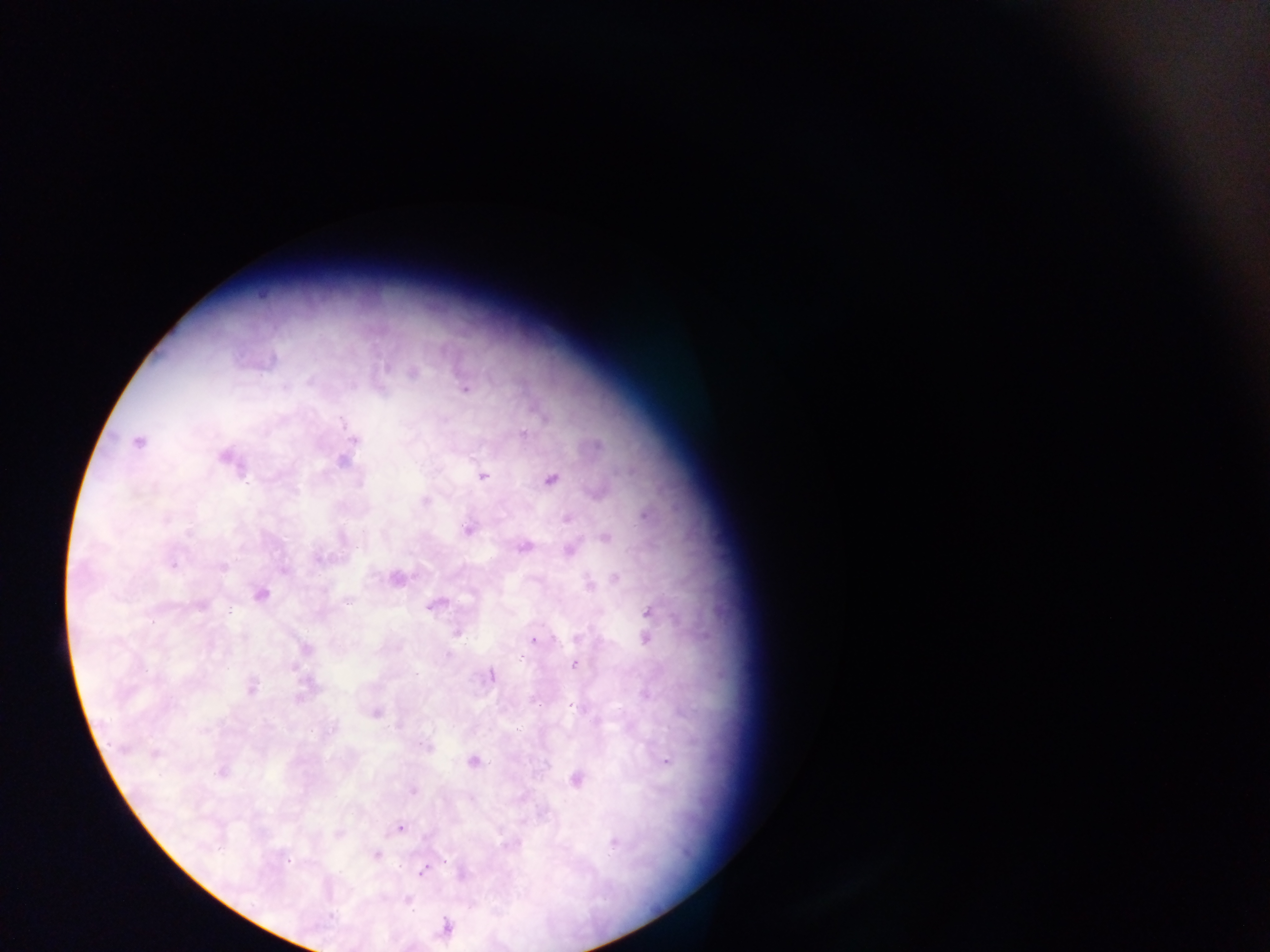

Approximate centers as [x, y] in pixels.
Summary:
  - Malaria parasite locations: [413, 373], [465, 388], [352, 441], [138, 442], [594, 445], [227, 457], [344, 458], [482, 476], [551, 479], [425, 501], [568, 518], [468, 528], [606, 536], [523, 546], [570, 549], [396, 578], [616, 579], [259, 594], [434, 603], [199, 605], [648, 611], [456, 631], [645, 635], [535, 639], [304, 649], [575, 664], [490, 675], [251, 687], [375, 712], [427, 745], [155, 754], [473, 762], [220, 770], [575, 779], [412, 789], [400, 827], [338, 833], [510, 843], [375, 854], [423, 869], [462, 872], [407, 900], [445, 928]
  - Preparation: thick blood film
  - Capture: mobile-phone photograph through a microscope
  - Field of view: single
  - Image size: 1270×952 pixels
  - Country: Ghana